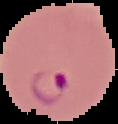

image size = 118×124 pixels
preparation = thin blood film
result = malaria parasites identified
image type = segmented cell region with the area outside set to black